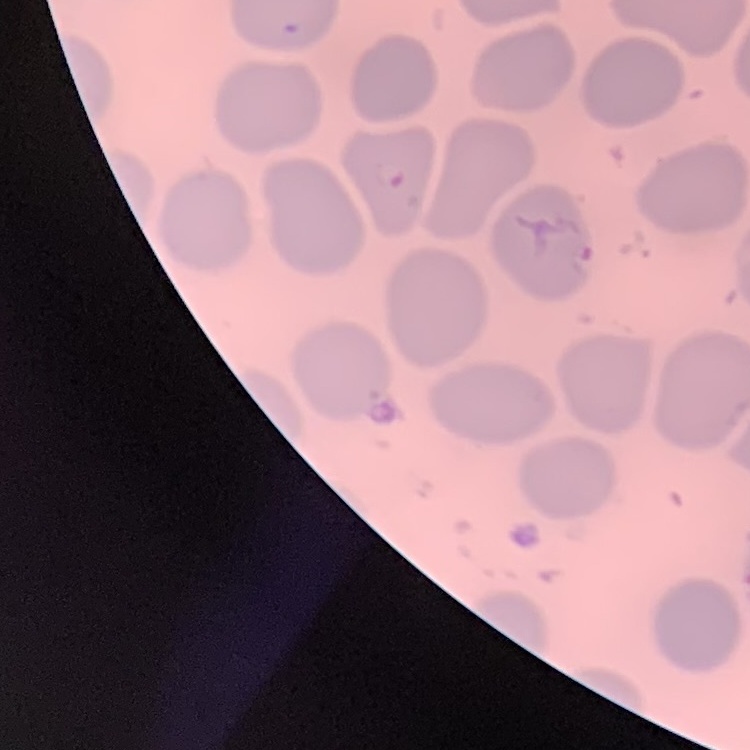

Summary:
  - Erythrocyte morphology: no rouleaux formation
  - Image type: square crop of a larger photomicrograph
  - Stain: Field's or Giemsa
  - Preparation: thin peripheral smear